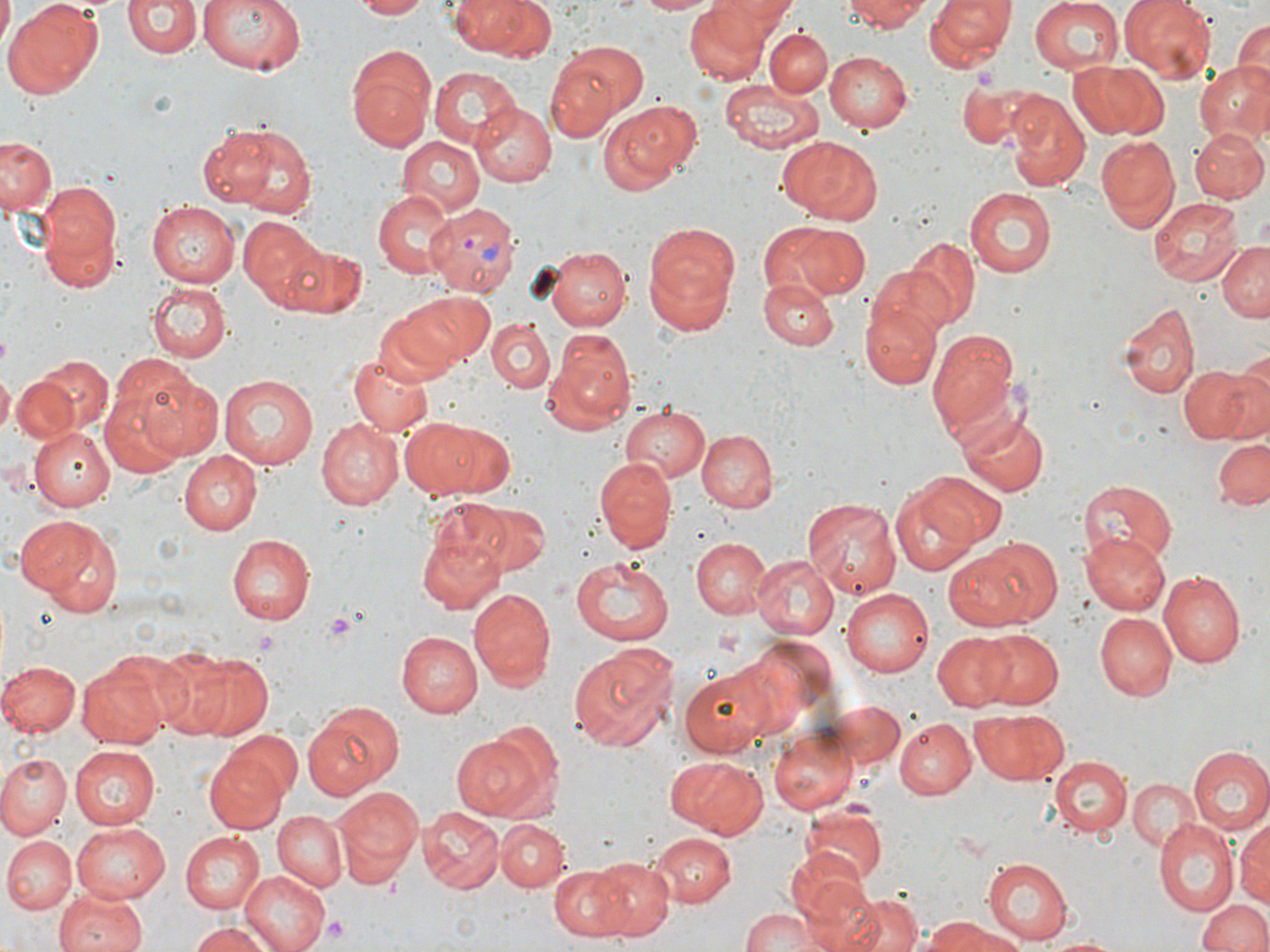

Approximate bounding boxes as named x1/y1/x2/y2 corners in pixels. Uninfected red blood cell locations: (x1=6, y1=0, x2=104, y2=96), (x1=124, y1=0, x2=200, y2=58), (x1=193, y1=0, x2=310, y2=77), (x1=353, y1=0, x2=431, y2=19), (x1=447, y1=0, x2=561, y2=62), (x1=628, y1=0, x2=725, y2=15), (x1=711, y1=0, x2=796, y2=33), (x1=845, y1=0, x2=930, y2=32), (x1=923, y1=0, x2=1018, y2=71), (x1=1027, y1=0, x2=1125, y2=77), (x1=1118, y1=0, x2=1218, y2=82), (x1=0, y1=1, x2=14, y2=44), (x1=683, y1=4, x2=773, y2=85), (x1=1232, y1=18, x2=1270, y2=93), (x1=765, y1=30, x2=833, y2=97), (x1=553, y1=41, x2=651, y2=122), (x1=346, y1=47, x2=436, y2=154), (x1=825, y1=51, x2=913, y2=134), (x1=546, y1=59, x2=618, y2=142), (x1=1069, y1=60, x2=1169, y2=141), (x1=1193, y1=61, x2=1269, y2=145), (x1=429, y1=66, x2=518, y2=147), (x1=721, y1=78, x2=824, y2=154), (x1=957, y1=83, x2=1045, y2=148), (x1=1007, y1=93, x2=1089, y2=190), (x1=599, y1=101, x2=700, y2=195), (x1=472, y1=105, x2=556, y2=188), (x1=209, y1=119, x2=319, y2=219), (x1=1190, y1=126, x2=1269, y2=201), (x1=1, y1=135, x2=58, y2=215), (x1=780, y1=135, x2=883, y2=224), (x1=397, y1=136, x2=485, y2=215), (x1=1095, y1=136, x2=1179, y2=231), (x1=381, y1=151, x2=474, y2=256), (x1=33, y1=182, x2=125, y2=289), (x1=964, y1=187, x2=1058, y2=279), (x1=373, y1=191, x2=454, y2=276), (x1=1151, y1=198, x2=1244, y2=286), (x1=149, y1=200, x2=243, y2=288), (x1=238, y1=215, x2=325, y2=311), (x1=643, y1=222, x2=739, y2=335), (x1=772, y1=223, x2=867, y2=299), (x1=904, y1=236, x2=981, y2=329), (x1=1216, y1=240, x2=1270, y2=323), (x1=278, y1=242, x2=368, y2=318), (x1=539, y1=246, x2=630, y2=328), (x1=759, y1=279, x2=838, y2=349), (x1=149, y1=280, x2=230, y2=361), (x1=392, y1=292, x2=491, y2=371), (x1=863, y1=297, x2=942, y2=392), (x1=1118, y1=303, x2=1199, y2=399), (x1=372, y1=311, x2=462, y2=388), (x1=485, y1=318, x2=554, y2=393), (x1=925, y1=327, x2=1023, y2=446), (x1=552, y1=331, x2=636, y2=424), (x1=347, y1=351, x2=435, y2=437), (x1=35, y1=354, x2=111, y2=431), (x1=109, y1=355, x2=198, y2=431), (x1=1178, y1=362, x2=1269, y2=446), (x1=0, y1=371, x2=15, y2=434), (x1=11, y1=372, x2=79, y2=443), (x1=138, y1=372, x2=225, y2=459), (x1=219, y1=373, x2=318, y2=469), (x1=103, y1=377, x2=199, y2=474), (x1=619, y1=404, x2=708, y2=484), (x1=961, y1=409, x2=1048, y2=499), (x1=400, y1=416, x2=515, y2=499), (x1=316, y1=418, x2=402, y2=511), (x1=27, y1=427, x2=115, y2=510), (x1=695, y1=428, x2=778, y2=513), (x1=1211, y1=436, x2=1270, y2=511), (x1=179, y1=451, x2=261, y2=535), (x1=594, y1=458, x2=679, y2=551), (x1=917, y1=471, x2=1007, y2=546), (x1=1079, y1=480, x2=1177, y2=564), (x1=891, y1=486, x2=983, y2=577), (x1=444, y1=498, x2=550, y2=576), (x1=803, y1=498, x2=903, y2=600), (x1=15, y1=514, x2=125, y2=614), (x1=417, y1=530, x2=504, y2=614), (x1=231, y1=531, x2=316, y2=623), (x1=1080, y1=532, x2=1170, y2=616), (x1=691, y1=536, x2=771, y2=616), (x1=961, y1=537, x2=1062, y2=628), (x1=751, y1=555, x2=839, y2=638), (x1=571, y1=557, x2=675, y2=644), (x1=1159, y1=570, x2=1246, y2=667), (x1=468, y1=586, x2=558, y2=691), (x1=838, y1=587, x2=934, y2=678), (x1=1094, y1=612, x2=1176, y2=701), (x1=394, y1=630, x2=481, y2=718), (x1=979, y1=631, x2=1064, y2=710), (x1=931, y1=632, x2=1017, y2=711), (x1=729, y1=641, x2=822, y2=739), (x1=567, y1=645, x2=676, y2=753), (x1=146, y1=646, x2=233, y2=734), (x1=180, y1=651, x2=274, y2=741), (x1=77, y1=659, x2=172, y2=749), (x1=0, y1=660, x2=79, y2=737), (x1=679, y1=667, x2=771, y2=756), (x1=819, y1=698, x2=907, y2=775), (x1=304, y1=699, x2=406, y2=800), (x1=969, y1=708, x2=1066, y2=786), (x1=895, y1=718, x2=976, y2=800), (x1=771, y1=726, x2=861, y2=816), (x1=221, y1=731, x2=303, y2=808), (x1=450, y1=731, x2=551, y2=820), (x1=70, y1=745, x2=162, y2=829), (x1=203, y1=747, x2=290, y2=834), (x1=1187, y1=747, x2=1270, y2=834), (x1=665, y1=753, x2=769, y2=838), (x1=0, y1=754, x2=73, y2=837), (x1=1049, y1=757, x2=1131, y2=838), (x1=1126, y1=778, x2=1201, y2=853), (x1=330, y1=784, x2=423, y2=889), (x1=421, y1=805, x2=504, y2=893), (x1=272, y1=810, x2=347, y2=893), (x1=804, y1=811, x2=886, y2=886), (x1=1233, y1=815, x2=1270, y2=909), (x1=496, y1=816, x2=569, y2=890), (x1=1152, y1=819, x2=1240, y2=917), (x1=72, y1=823, x2=171, y2=903), (x1=648, y1=831, x2=735, y2=908), (x1=181, y1=832, x2=263, y2=912), (x1=2, y1=835, x2=75, y2=913), (x1=610, y1=842, x2=724, y2=930), (x1=788, y1=848, x2=871, y2=922), (x1=586, y1=857, x2=674, y2=940), (x1=983, y1=857, x2=1071, y2=943), (x1=548, y1=864, x2=636, y2=940), (x1=240, y1=868, x2=336, y2=952), (x1=802, y1=879, x2=887, y2=952), (x1=55, y1=886, x2=148, y2=952), (x1=833, y1=893, x2=923, y2=952), (x1=1197, y1=895, x2=1269, y2=952), (x1=738, y1=909, x2=825, y2=952), (x1=920, y1=916, x2=1004, y2=951), (x1=185, y1=920, x2=278, y2=952), (x1=946, y1=926, x2=1029, y2=952), (x1=1041, y1=932, x2=1125, y2=952). Platelet locations: (x1=320, y1=611, x2=361, y2=645), (x1=324, y1=914, x2=349, y2=942). Plasmodium vivax-infected red blood cell locations: (x1=429, y1=205, x2=520, y2=294). Slide-level diagnosis: Plasmodium vivax. Captured at 1000x magnification. Thin blood smear. Image is 1270×952 pixels. May-Grünwald-Giemsa-stained preparation. One field of a larger specimen. Optical microscopy.